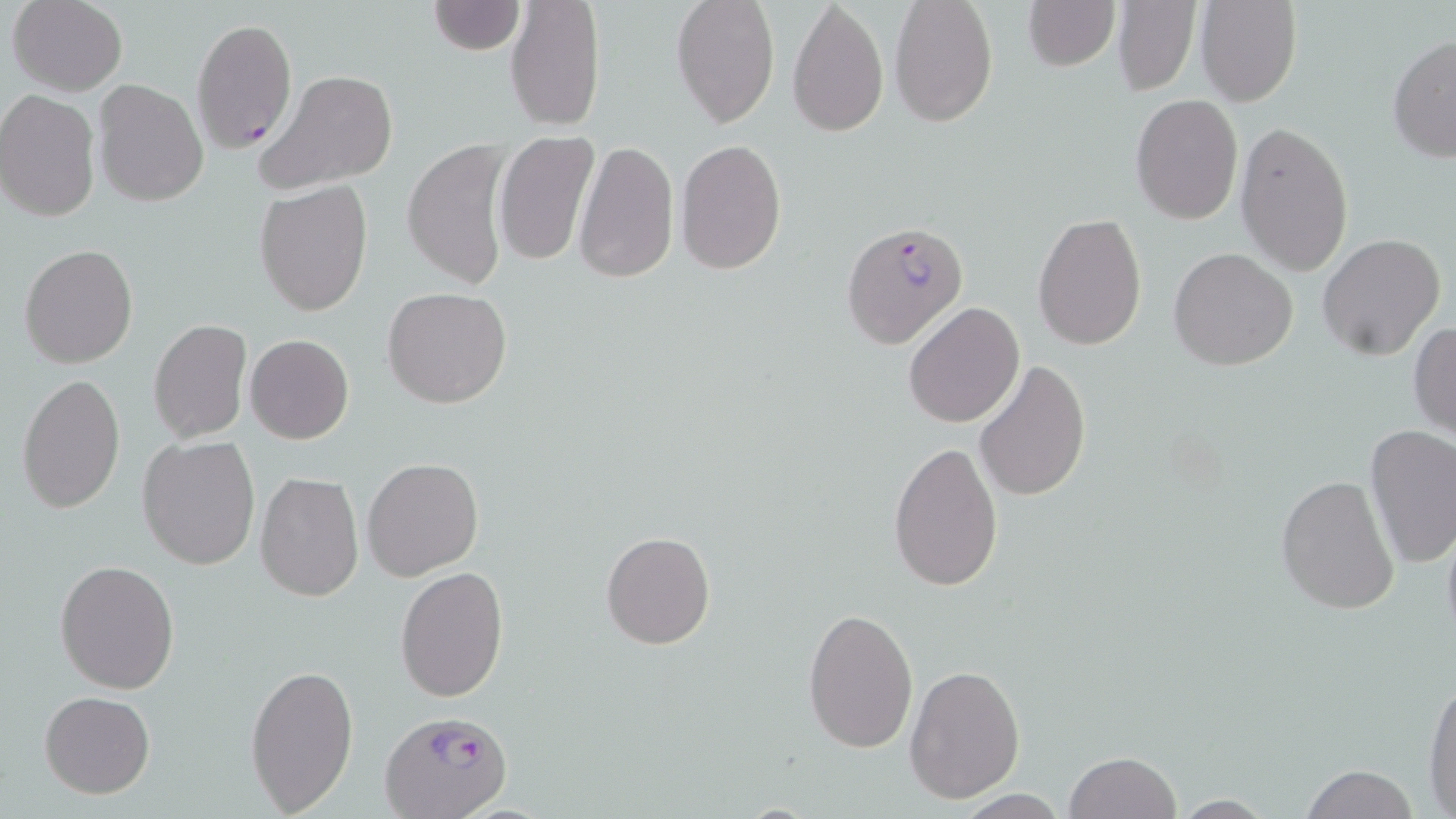

Approximate bounding boxes as (x1, y1, x2, y2) in pixels. Plasmodium falciparum-infected red blood cell locations: (191, 18, 297, 154), (841, 221, 970, 350), (380, 708, 512, 819). Uninfected red blood cell locations: (7, 0, 128, 96), (506, 0, 605, 131), (670, 0, 781, 129), (787, 0, 889, 138), (888, 0, 999, 128), (1022, 0, 1120, 71), (1195, 0, 1302, 107), (428, 1, 522, 55), (1111, 1, 1203, 96), (1387, 34, 1456, 163), (255, 69, 400, 194), (95, 79, 208, 209), (0, 89, 100, 221), (1131, 94, 1242, 223), (1234, 120, 1354, 274), (494, 132, 598, 267), (403, 138, 513, 290), (675, 139, 787, 275), (573, 140, 679, 286), (256, 181, 373, 317), (1033, 214, 1147, 351), (1316, 233, 1445, 361), (19, 244, 138, 368), (1168, 247, 1298, 372), (381, 287, 512, 409), (903, 301, 1024, 428), (147, 319, 252, 444), (1409, 322, 1456, 442), (244, 335, 354, 444), (973, 359, 1089, 503), (15, 373, 126, 513), (1363, 427, 1456, 568), (137, 437, 260, 570), (888, 439, 1003, 592), (362, 457, 484, 581), (254, 472, 364, 603), (1274, 472, 1401, 613), (1440, 517, 1456, 646), (600, 531, 715, 650), (55, 559, 181, 693), (394, 566, 509, 703), (802, 606, 919, 752), (245, 663, 358, 815), (904, 663, 1026, 804), (1422, 671, 1455, 813), (40, 691, 155, 797), (1064, 750, 1181, 819), (1297, 762, 1420, 819), (1170, 795, 1280, 816). Slide-level diagnosis: Plasmodium falciparum. One field of a larger specimen. Captured at 1000x magnification. Light microscopy. Thin blood film. Image is 1456×819 pixels. May-Grünwald-Giemsa stain.